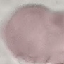

malaria status = uninfected
capture = smartphone through the microscope eyepiece
preparation = thin blood smear
stain = Giemsa
image type = cell patch, automatically extracted from a larger field of view and resized to 64 × 64 pixels